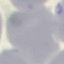 Result: no malaria parasites seen. Thin blood smear. Giemsa-stained preparation. Acquired by smartphone through the microscope eyepiece. Cell patch, automatically extracted from a larger field of view and resized to 64 × 64 pixels.